Classify this cell by malaria status.
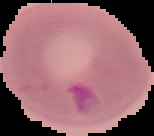
Parasitized.

From a thin blood smear. Image is 154×136 pixels. The area outside the segmented cell region is set to black.